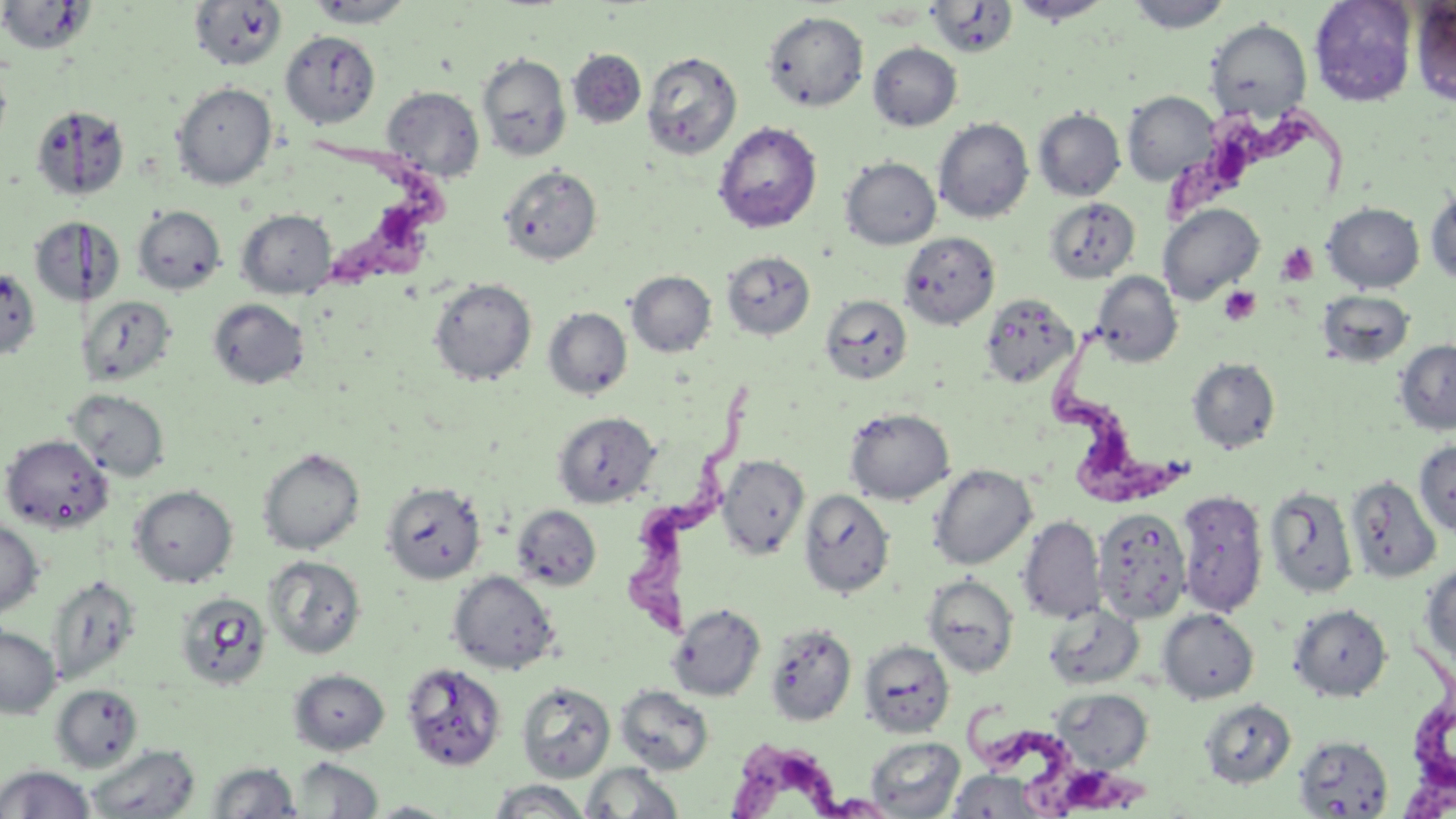

Approximate bounding boxes as (x1, y1, x2, y2) in pixels. Uninfected red blood cell locations: (1, 0, 95, 57), (303, 0, 417, 27), (1008, 0, 1114, 25), (1125, 0, 1232, 33), (1309, 0, 1417, 106), (188, 1, 288, 72), (926, 1, 1018, 59), (1409, 1, 1456, 106), (763, 10, 868, 112), (1206, 19, 1311, 120), (280, 30, 380, 127), (867, 42, 962, 131), (567, 49, 646, 129), (641, 50, 743, 161), (477, 52, 571, 162), (0, 58, 12, 154), (172, 82, 277, 189), (382, 86, 484, 181), (1122, 91, 1219, 185), (31, 104, 129, 202), (1034, 107, 1125, 201), (933, 117, 1034, 223), (713, 121, 822, 233), (841, 157, 941, 249), (499, 164, 602, 265), (1425, 187, 1456, 286), (1043, 198, 1139, 284), (1322, 202, 1424, 293), (1158, 203, 1264, 302), (132, 205, 226, 295), (236, 209, 336, 299), (29, 216, 82, 308), (84, 217, 124, 307), (899, 231, 999, 329), (721, 251, 815, 339), (0, 267, 40, 360), (626, 270, 716, 357), (1092, 271, 1182, 367), (429, 277, 537, 385), (1319, 291, 1414, 366), (83, 294, 176, 386), (821, 294, 912, 384), (980, 294, 1077, 388), (208, 298, 309, 389), (543, 307, 632, 399), (1394, 339, 1456, 434), (1187, 357, 1281, 453), (67, 388, 170, 481), (844, 407, 955, 505), (553, 411, 660, 508), (1, 434, 113, 532), (1414, 439, 1456, 537), (258, 448, 365, 555), (716, 454, 809, 559), (928, 465, 1037, 570), (1345, 475, 1442, 586), (382, 482, 486, 585), (129, 485, 237, 587), (1264, 486, 1358, 599), (799, 488, 895, 598), (1175, 489, 1268, 617), (512, 505, 601, 591), (1093, 508, 1192, 623), (1018, 516, 1106, 624), (0, 519, 44, 616), (264, 555, 366, 659), (1420, 561, 1456, 671), (448, 570, 559, 674), (923, 574, 1019, 677), (47, 575, 141, 686), (174, 590, 272, 691), (667, 603, 766, 701), (1289, 603, 1392, 701), (1043, 604, 1145, 691), (1158, 609, 1259, 703), (765, 623, 856, 726), (0, 624, 60, 718), (859, 640, 954, 737), (401, 661, 506, 771), (289, 668, 389, 754), (517, 680, 616, 782), (50, 683, 143, 772), (615, 684, 714, 776), (1051, 688, 1153, 773), (1202, 695, 1299, 785), (1292, 734, 1393, 817), (866, 736, 965, 817), (86, 744, 201, 818), (291, 757, 384, 817), (207, 761, 301, 818), (581, 762, 684, 818), (0, 764, 96, 818), (946, 770, 1050, 818), (487, 780, 592, 817), (364, 800, 460, 818). Platelet locations: (1276, 242, 1319, 286), (1219, 285, 1261, 326). Trypanosoma brucei locations: (1157, 96, 1359, 227), (310, 129, 450, 297), (1040, 322, 1204, 502), (627, 384, 753, 644), (1396, 635, 1456, 817), (963, 700, 1170, 819), (727, 743, 892, 819). Slide-level diagnosis: Trypanosoma brucei. Image is 1456×819 pixels. Thin blood smear. Optical microscopy. One field of a larger specimen. Captured at 1000x magnification. May-Grünwald-Giemsa stain.